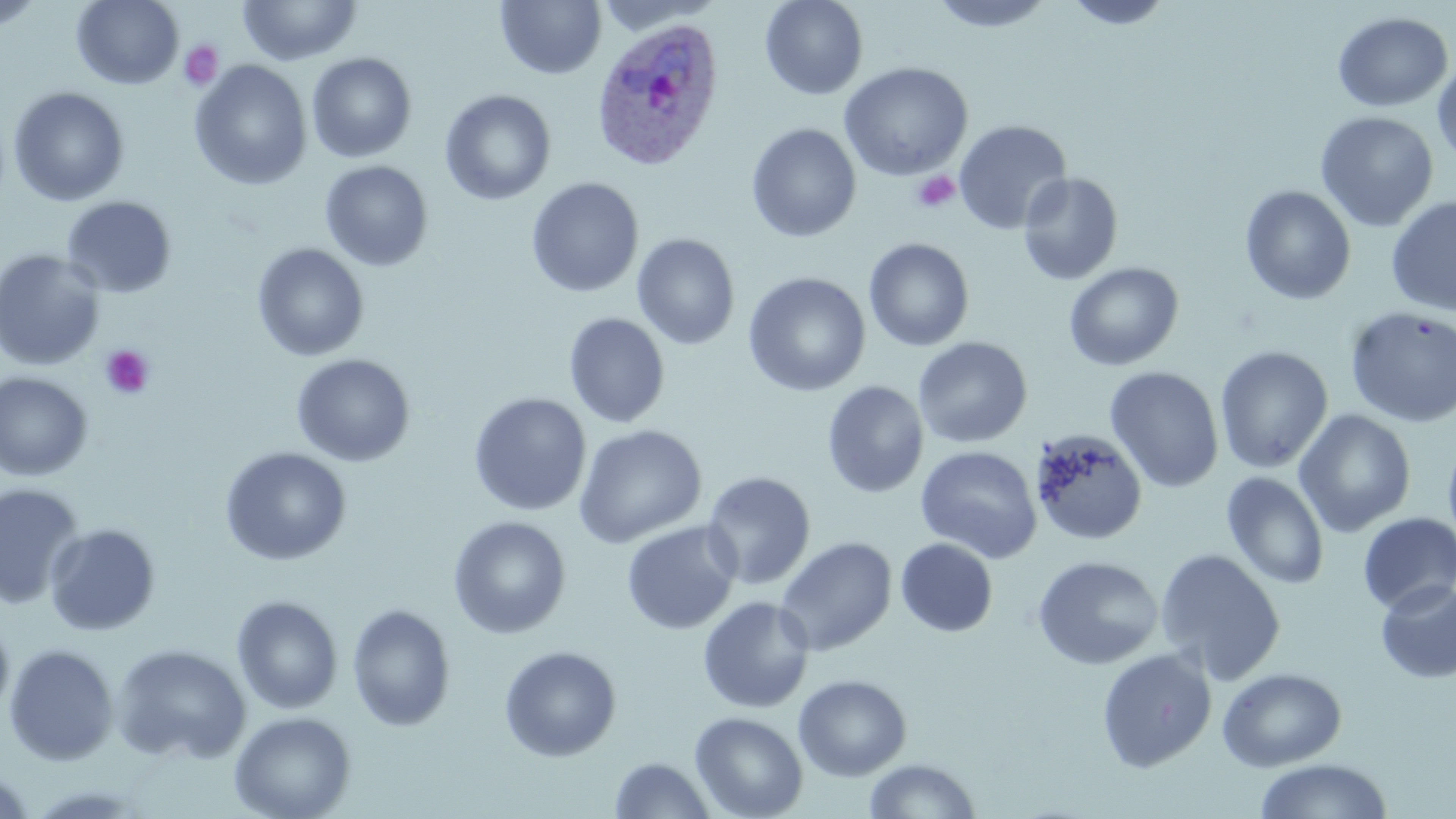

slide_level_diagnosis: Plasmodium ovale
field_of_view: single
plasmodium_ovale_infected_red_blood_cell_locations: 'approximate bounding boxes as [x1, y1, x2, y2] in pixels: [591, 16, 726, 172]'
stain: May-Grünwald-Giemsa
image_size: 1456×819 pixels
platelet_locations: 'approximate bounding boxes as [x1, y1, x2, y2] in pixels: [179, 40, 223, 91], [911, 170, 961, 214], [99, 345, 155, 400]'
modality: light microscopy
preparation: thin blood film
uninfected_red_blood_cell_locations: 'approximate bounding boxes as [x1, y1, x2, y2] in pixels: [0, 0, 44, 32], [72, 0, 184, 90], [237, 0, 363, 66], [495, 0, 606, 80], [760, 0, 868, 100], [928, 0, 1058, 33], [1062, 0, 1175, 29], [593, 1, 724, 35], [1332, 11, 1453, 112], [307, 52, 417, 163], [1432, 58, 1456, 164], [191, 60, 312, 189], [839, 61, 974, 181], [8, 86, 129, 206], [440, 89, 557, 206], [1315, 111, 1439, 231], [953, 119, 1073, 235], [746, 123, 862, 243], [320, 160, 433, 271], [1018, 172, 1124, 286], [526, 177, 644, 298], [1240, 185, 1356, 304], [61, 196, 178, 298], [1386, 196, 1456, 316], [632, 233, 740, 350], [863, 238, 975, 352], [252, 243, 369, 361], [0, 249, 106, 371], [1064, 262, 1184, 371], [743, 272, 871, 396], [1345, 306, 1456, 427], [563, 312, 670, 428], [913, 336, 1032, 449], [1215, 345, 1333, 473], [291, 353, 415, 467], [1104, 366, 1224, 493], [0, 371, 94, 482], [822, 380, 929, 498], [468, 392, 592, 516], [1294, 409, 1416, 538], [573, 424, 707, 549], [1030, 428, 1148, 545], [1443, 432, 1456, 558], [914, 444, 1043, 563], [219, 446, 352, 565], [701, 471, 816, 590], [1221, 471, 1330, 590], [1, 484, 85, 609], [1358, 513, 1456, 614], [447, 515, 571, 639], [621, 520, 741, 635], [44, 523, 161, 636], [774, 536, 897, 657], [895, 538, 998, 637], [1154, 547, 1286, 684], [1032, 555, 1164, 670], [1375, 579, 1456, 684], [231, 595, 343, 714], [697, 596, 815, 713], [347, 603, 457, 731], [0, 618, 14, 722], [4, 643, 119, 766], [110, 643, 251, 764], [499, 645, 621, 761], [1096, 648, 1217, 772], [1217, 666, 1347, 771], [793, 674, 912, 781], [229, 710, 356, 819], [690, 711, 808, 818], [609, 757, 716, 818], [1253, 757, 1394, 819], [863, 758, 981, 818], [1, 768, 36, 817]'
magnification: 1000x